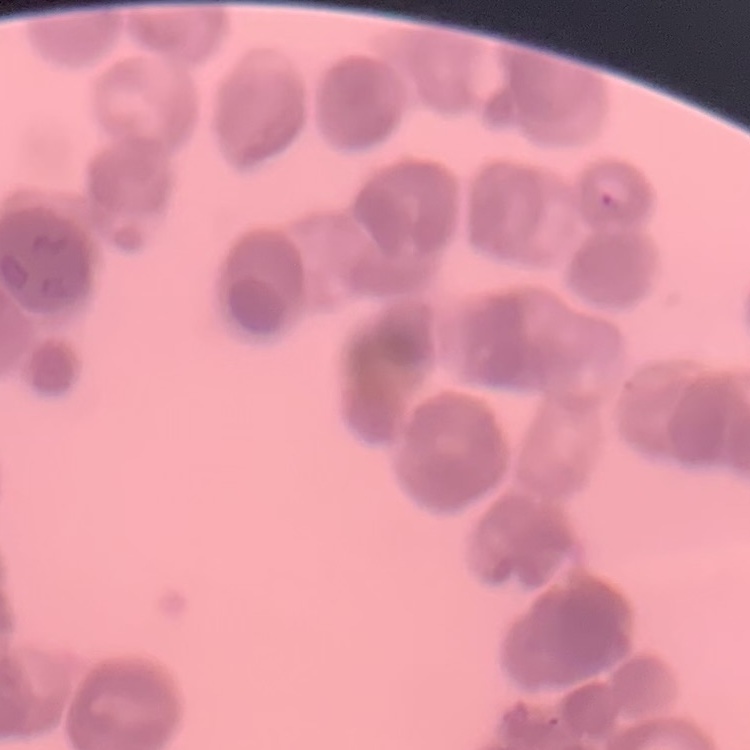
Summary:
  - Red blood cell morphology: rouleaux formation
  - Image type: one tile cut from a larger photomicrograph
  - Stain: Field's or Giemsa
  - Preparation: thin peripheral smear